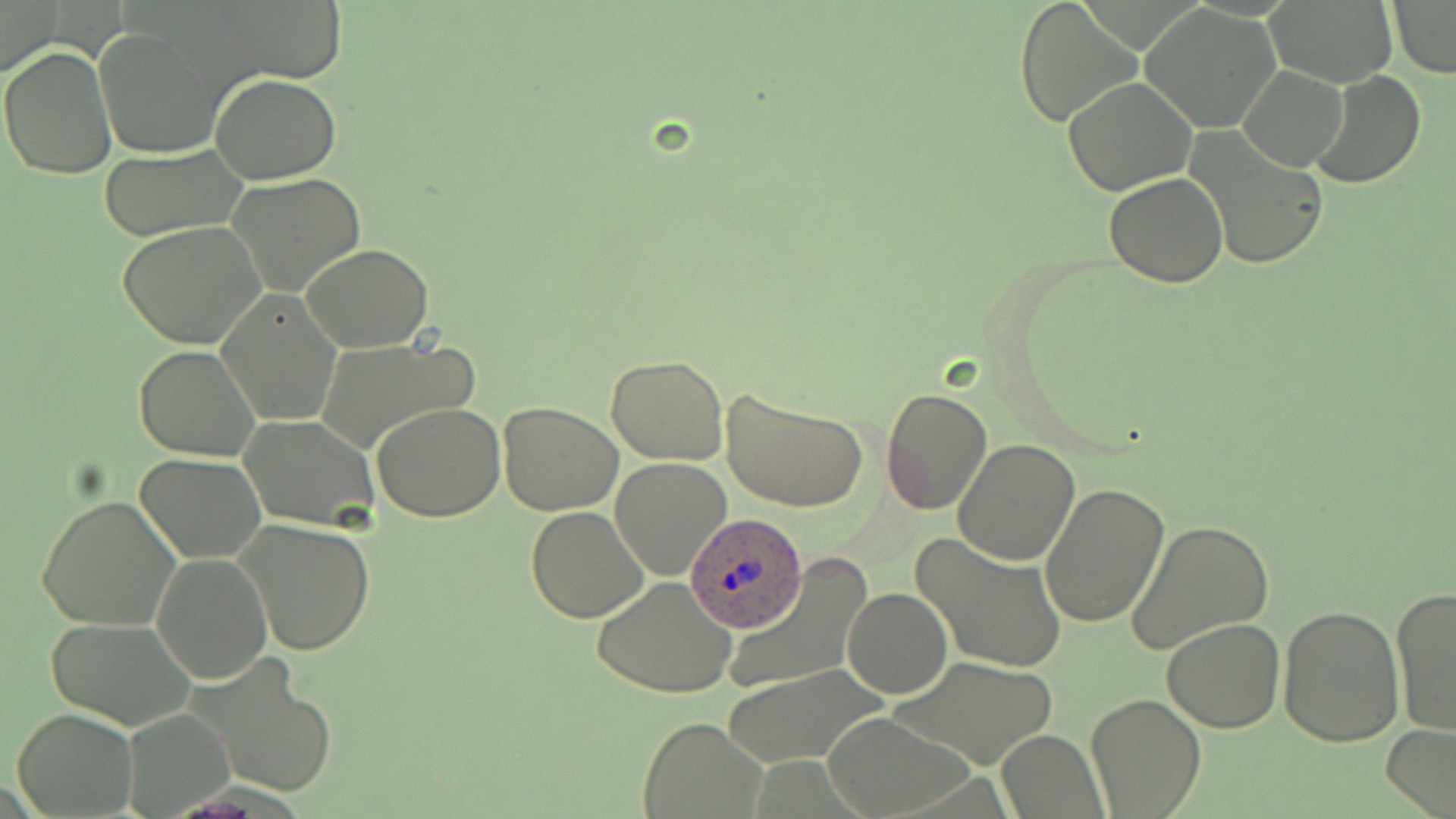
slide-level diagnosis = Plasmodium ovale
preparation = thin blood smear
Plasmodium ovale-infected red blood cell locations = approximate bounding boxes as named x1/y1/x2/y2 corners in pixels: (x1=687, y1=516, x2=803, y2=639)
field of view = single
magnification = 1000x
uninfected red blood cell locations = approximate bounding boxes as named x1/y1/x2/y2 corners in pixels: (x1=211, y1=0, x2=350, y2=83), (x1=1012, y1=0, x2=1141, y2=128), (x1=1387, y1=1, x2=1455, y2=78), (x1=1262, y1=2, x2=1399, y2=88), (x1=0, y1=3, x2=62, y2=78), (x1=1139, y1=4, x2=1283, y2=133), (x1=95, y1=29, x2=220, y2=160), (x1=1, y1=44, x2=116, y2=180), (x1=1238, y1=66, x2=1348, y2=171), (x1=1311, y1=72, x2=1426, y2=189), (x1=211, y1=73, x2=341, y2=183), (x1=1063, y1=76, x2=1198, y2=196), (x1=1186, y1=129, x2=1326, y2=271), (x1=98, y1=147, x2=246, y2=242), (x1=226, y1=174, x2=368, y2=298), (x1=1103, y1=174, x2=1230, y2=288), (x1=118, y1=221, x2=267, y2=351), (x1=301, y1=242, x2=434, y2=351), (x1=216, y1=290, x2=342, y2=426), (x1=313, y1=337, x2=482, y2=454), (x1=133, y1=345, x2=260, y2=460), (x1=605, y1=355, x2=729, y2=465), (x1=720, y1=385, x2=869, y2=513), (x1=880, y1=389, x2=993, y2=515), (x1=497, y1=401, x2=623, y2=516), (x1=373, y1=402, x2=505, y2=521), (x1=240, y1=414, x2=384, y2=530), (x1=951, y1=439, x2=1080, y2=566), (x1=136, y1=452, x2=265, y2=562), (x1=612, y1=458, x2=732, y2=579), (x1=1039, y1=480, x2=1169, y2=628), (x1=36, y1=493, x2=181, y2=633), (x1=526, y1=508, x2=650, y2=623), (x1=235, y1=517, x2=378, y2=656), (x1=1125, y1=519, x2=1274, y2=659), (x1=911, y1=531, x2=1067, y2=674), (x1=151, y1=552, x2=273, y2=684), (x1=729, y1=565, x2=868, y2=698), (x1=593, y1=578, x2=737, y2=697), (x1=841, y1=586, x2=952, y2=698), (x1=1391, y1=587, x2=1456, y2=735), (x1=1277, y1=602, x2=1404, y2=746), (x1=46, y1=617, x2=192, y2=732), (x1=1162, y1=617, x2=1287, y2=733), (x1=191, y1=657, x2=337, y2=799), (x1=888, y1=657, x2=1057, y2=770), (x1=720, y1=665, x2=889, y2=768), (x1=1087, y1=694, x2=1204, y2=818), (x1=120, y1=703, x2=236, y2=818), (x1=13, y1=708, x2=139, y2=818), (x1=820, y1=711, x2=973, y2=816), (x1=637, y1=716, x2=767, y2=817), (x1=1380, y1=723, x2=1456, y2=819), (x1=995, y1=730, x2=1107, y2=817)
modality = optical microscopy
image size = 1456×819 pixels
stain = May-Grünwald-Giemsa